Classify this cell by malaria status.
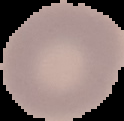
Uninfected.

preparation: thin blood smear
image_size: 124×121 pixels
image_type: cell region segmented out of the field of view; surrounding area masked to black